Name the parasite shown.
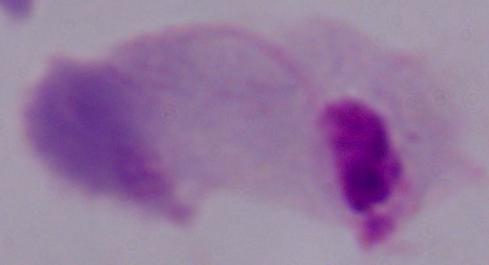
This is a trichomonad.

{
  "magnification": "1000x",
  "modality": "micrograph"
}